Name the parasite shown.
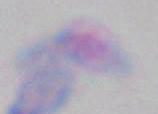

This is Toxoplasma gondii.

Summary:
  - Modality: photomicrograph
  - Magnification: 1000x